Identify the parasite.
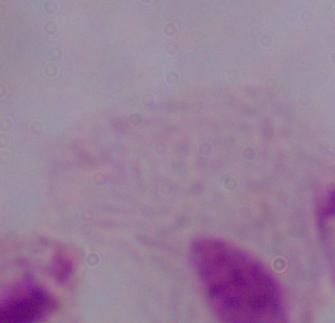
This is a trichomonad.

modality: micrograph
magnification: 1000x